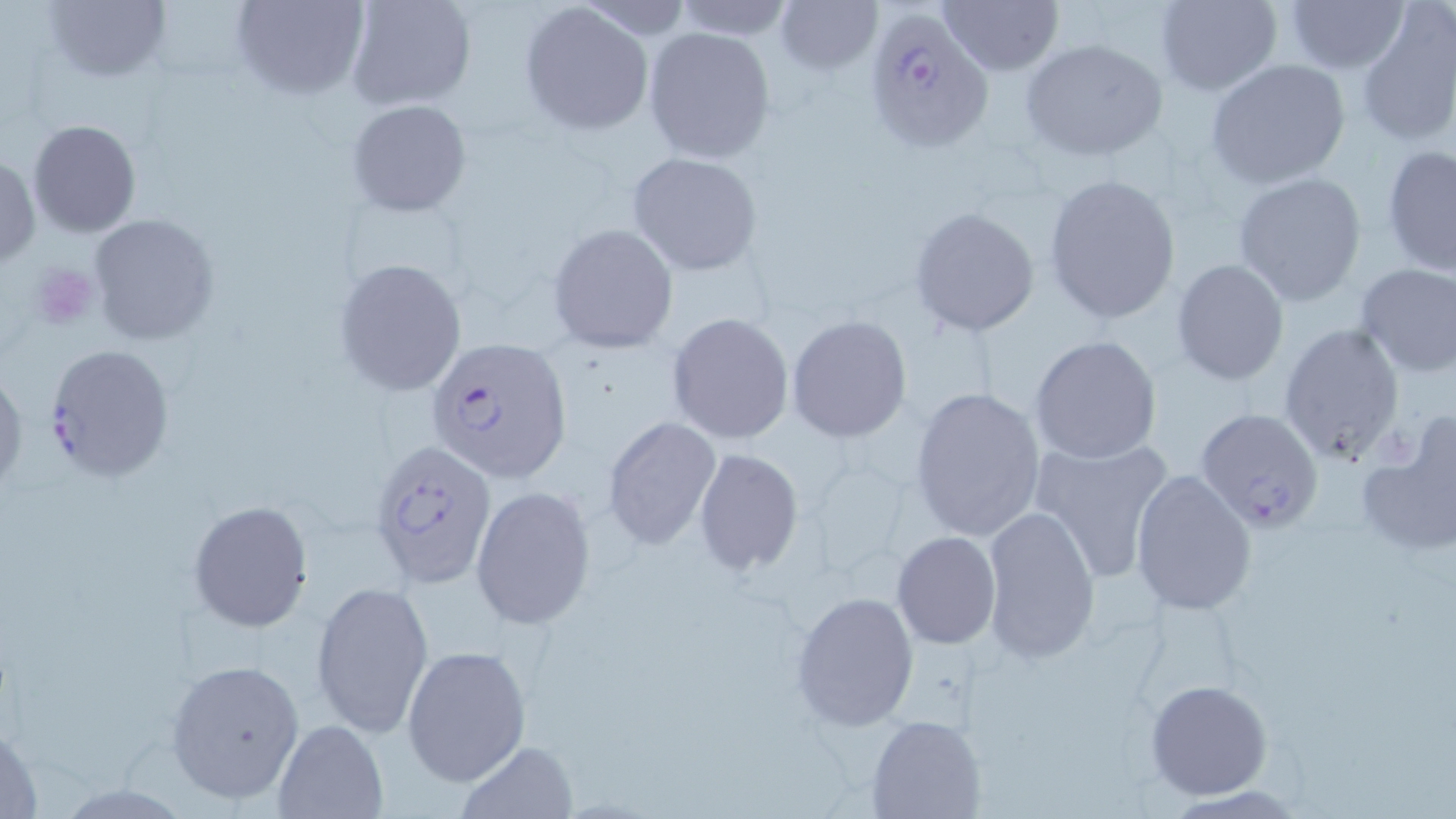
Approximate bounding boxes as (x1, y1, x2, y2) in pixels. Platelet locations: (29, 262, 99, 331). Uninfected red blood cell locations: (37, 0, 173, 85), (231, 0, 369, 100), (345, 0, 475, 110), (668, 0, 799, 41), (772, 0, 883, 76), (940, 0, 1063, 75), (1153, 0, 1283, 94), (1283, 0, 1410, 73), (519, 2, 654, 135), (1355, 8, 1456, 145), (643, 26, 777, 163), (1019, 38, 1169, 162), (1206, 58, 1352, 189), (346, 99, 472, 217), (27, 119, 142, 237), (1381, 144, 1456, 276), (1, 152, 40, 269), (626, 152, 765, 277), (1233, 171, 1366, 305), (1043, 173, 1182, 326), (908, 204, 1041, 338), (89, 214, 220, 345), (548, 222, 678, 353), (334, 258, 468, 397), (1171, 260, 1290, 386), (1353, 263, 1456, 378), (666, 311, 795, 444), (787, 315, 912, 442), (1277, 323, 1406, 467), (1030, 335, 1163, 466), (0, 367, 26, 500), (908, 385, 1046, 542), (1354, 414, 1456, 556), (603, 415, 721, 549), (1029, 437, 1176, 585), (694, 448, 805, 577), (1131, 470, 1257, 616), (471, 486, 596, 629), (187, 500, 314, 632), (982, 505, 1100, 665), (890, 531, 1002, 649), (311, 579, 434, 740), (792, 592, 919, 729), (401, 645, 531, 786), (167, 659, 307, 804), (1145, 679, 1273, 802), (867, 715, 984, 818), (271, 719, 388, 818), (459, 740, 577, 818). Plasmodium falciparum-infected red blood cell locations: (865, 8, 995, 152), (426, 338, 574, 483), (41, 343, 174, 482), (1194, 408, 1325, 532), (367, 438, 498, 589). Slide-level diagnosis: Plasmodium falciparum. 1000x magnification. Thin blood smear. One field of a larger specimen. May-Grünwald-Giemsa stain. Optical microscopy. Image is 1456×819 pixels.